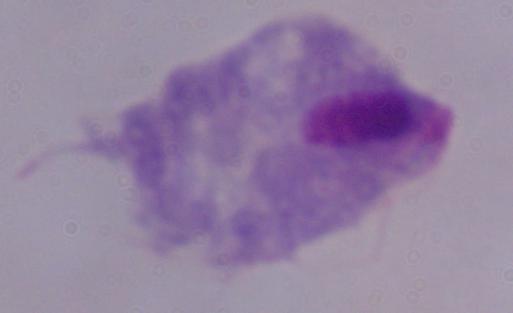
A trichomonad is shown. Micrograph. Captured at 1000x magnification.